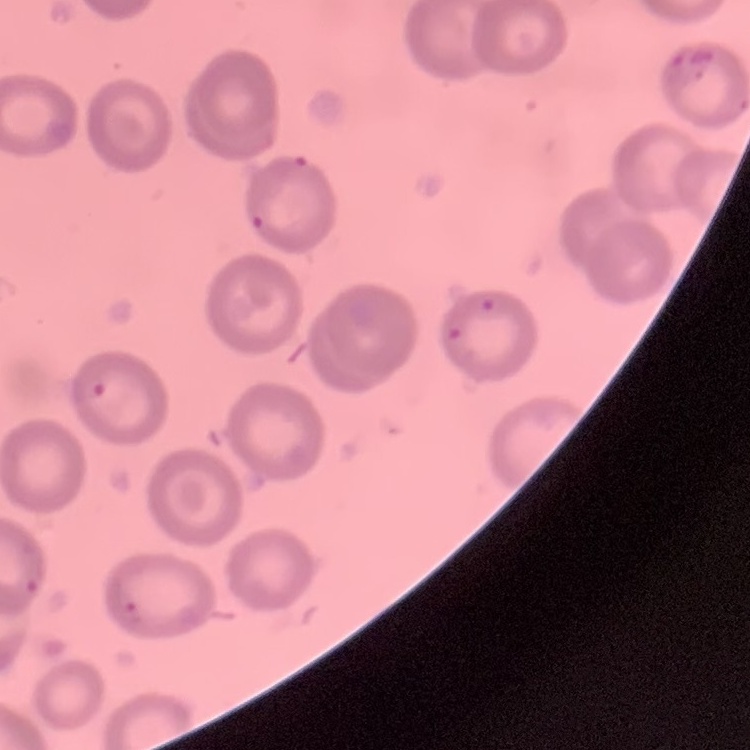

red blood cell morphology = no rouleaux formation
image type = one tile cut from a larger photomicrograph
preparation = thin blood smear
stain = Field's or Giemsa